Identify the parasite.
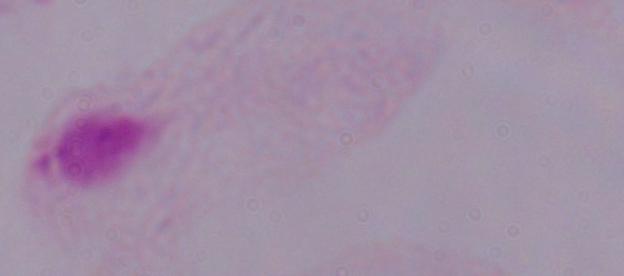

This is a trichomonad.

Summary:
  - Modality: micrograph
  - Magnification: 1000x